Name the parasite shown.
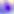

Toxoplasma gondii.

Summary:
  - Modality: photomicrograph
  - Magnification: 400x